Report the malaria status of this cell.
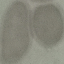
It is uninfected.

Cell patch, automatically extracted from a larger field of view and resized to 64 × 64 pixels. Thin smear of blood. Photographed with a smartphone camera at the microscope eyepiece. Giemsa-stained preparation.